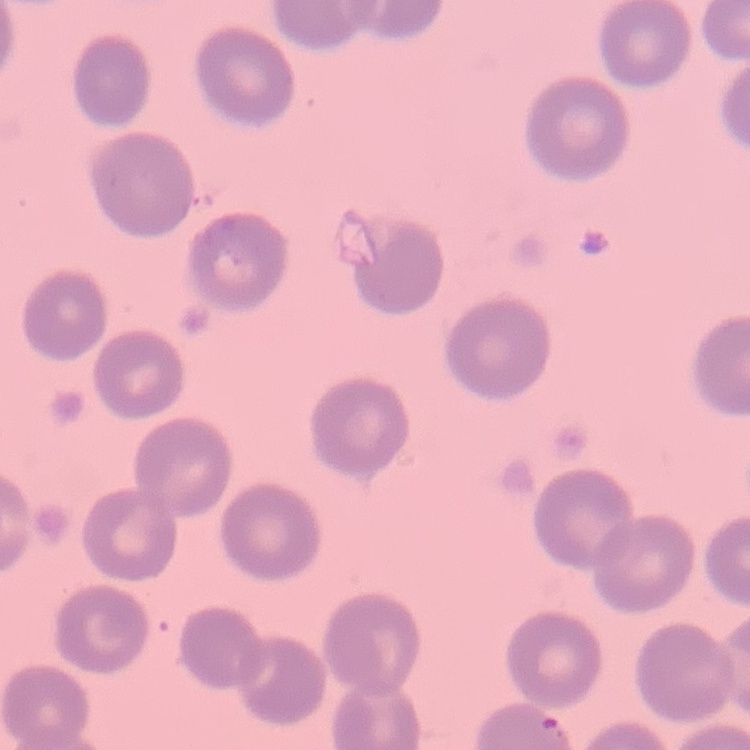
erythrocyte_morphology: no rouleaux formation
stain: Field's or Giemsa
preparation: thin blood smear
image_type: one tile cut from a larger photomicrograph